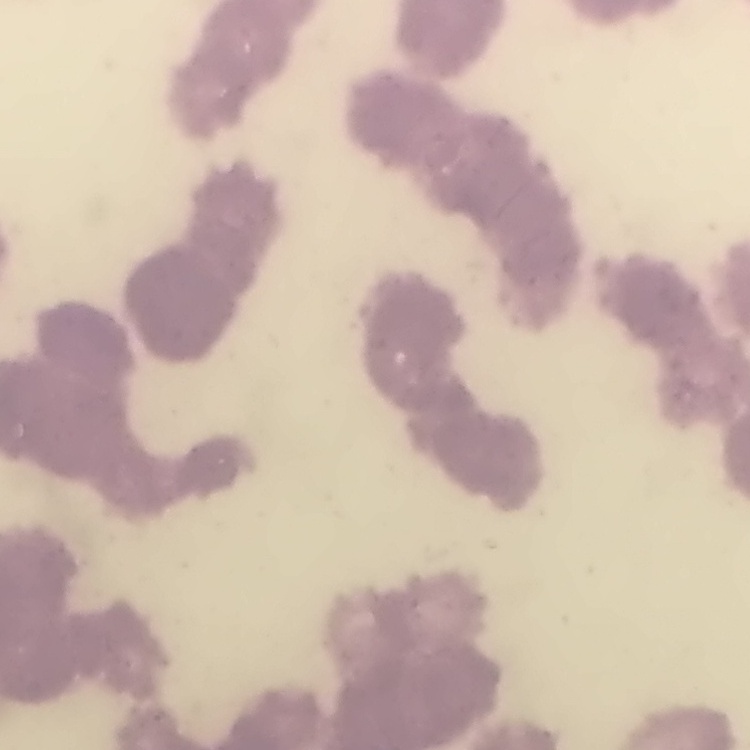
The erythrocytes exhibit rouleaux formation. Thin peripheral smear. One tile cut from a larger photomicrograph. Field's or Giemsa stain.